Assess this cell for malaria.
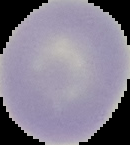

It is uninfected.

From a thin blood film. Cell region segmented out of the field of view; the surrounding area is masked to black. Image is 130×145 pixels.